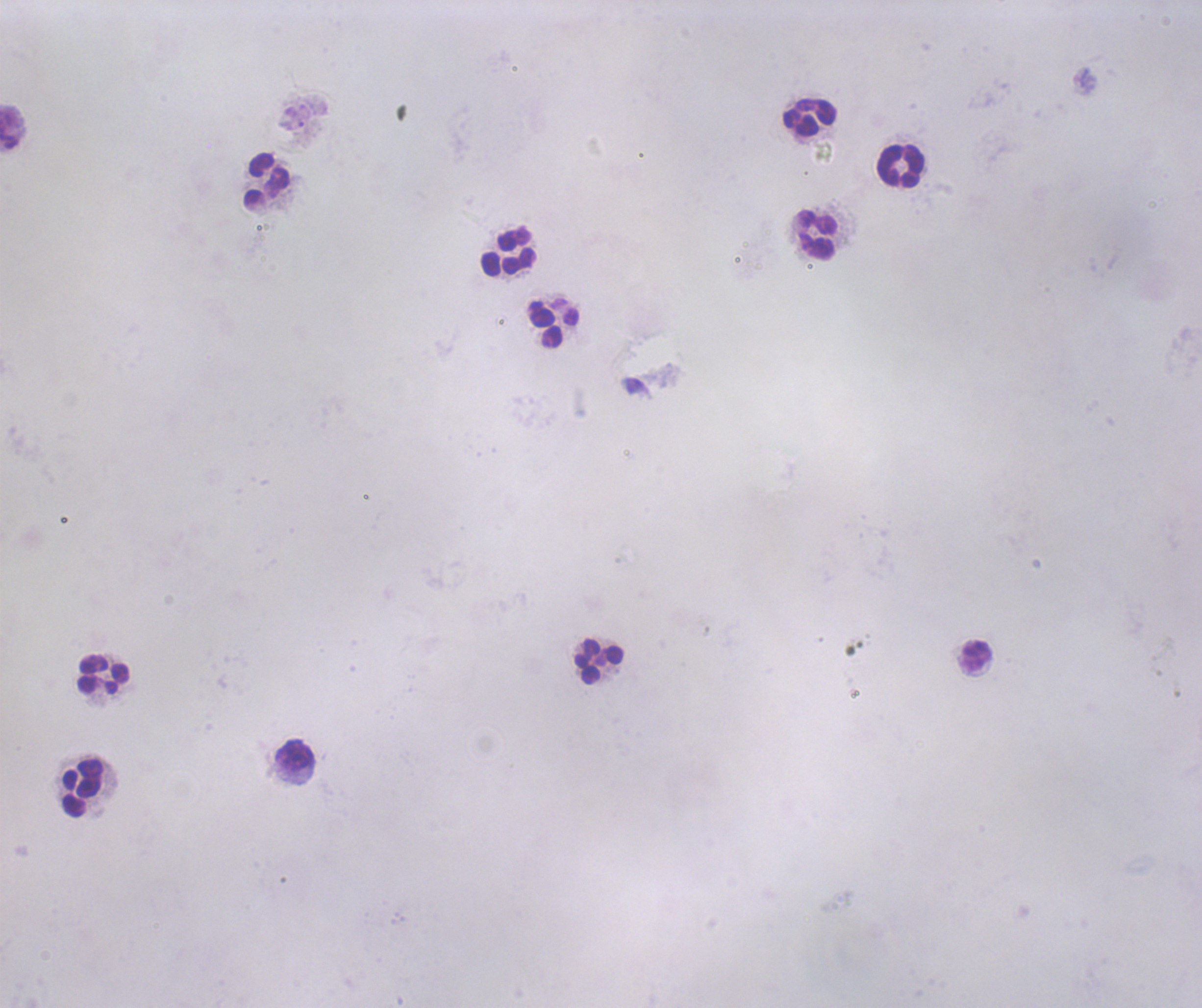
Approximate object centers, in pixels from the top-left corner.
Summary:
  - Leukocyte locations: (x=809, y=117), (x=900, y=166), (x=267, y=179), (x=817, y=235), (x=508, y=252), (x=554, y=328), (x=977, y=657), (x=599, y=662), (x=102, y=675), (x=295, y=755), (x=83, y=787)
  - Image size: 1202×1008 pixels
  - Background quality: unsatisfactory
  - Coloration quality: bad
  - Stain: Romanowsky
  - Result: negative for malaria parasites
  - Preparation: thick blood smear
  - Magnification: 100x
  - Context: previously used in a real diagnosis
  - Field of view: one from this slide